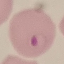
malaria status = parasitized
preparation = thin blood film
stain = Giemsa
capture = smartphone through the microscope eyepiece
image type = cell patch, automatically extracted from a larger field of view and resized to 64 × 64 pixels